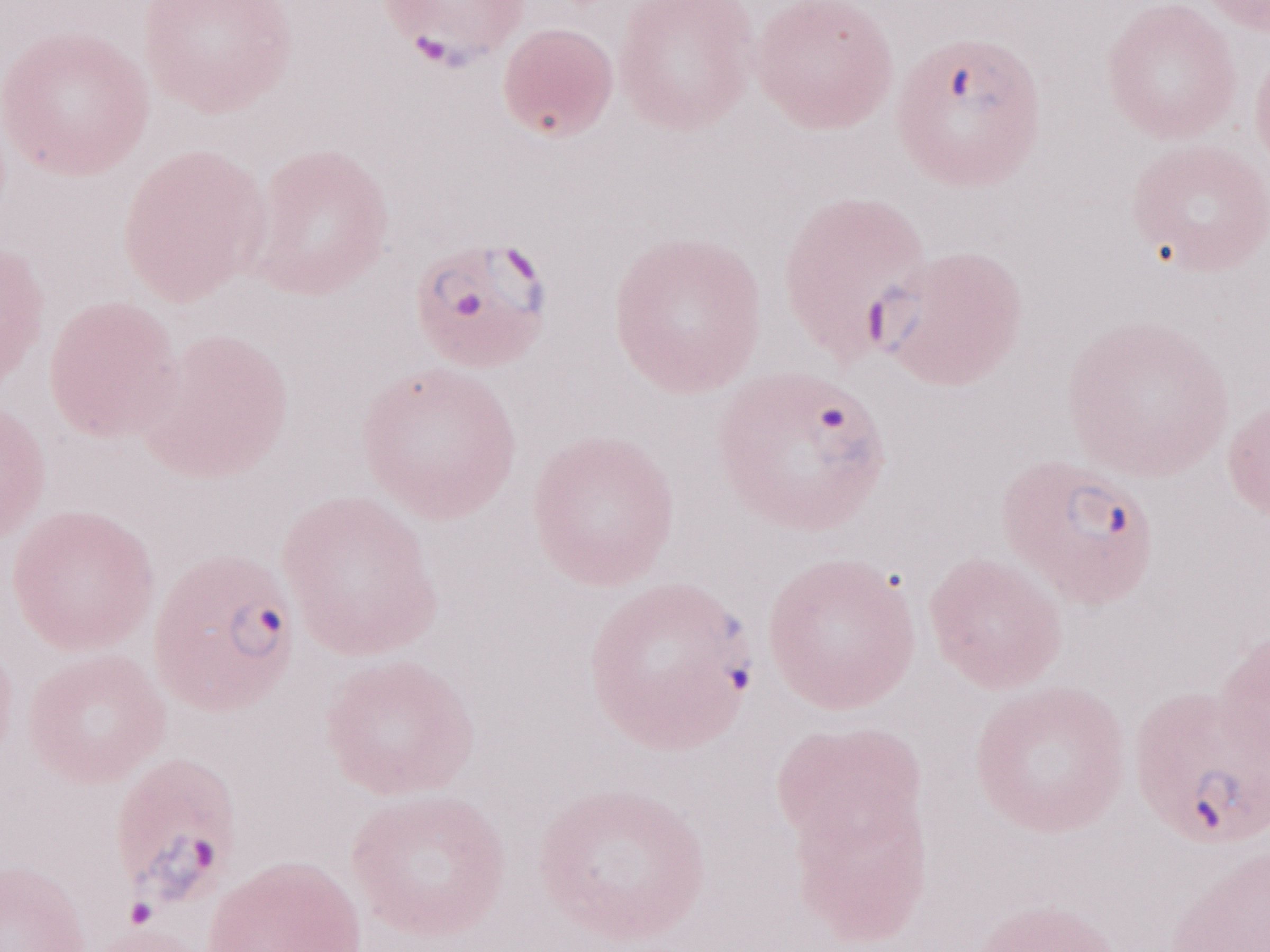

Single field of view. Olympus BX43 microscope and DP73 digital camera. Image is 1270×952 pixels. Thin blood film. 1,000x magnification. Malaria diagnosis (patient-level): positive. May-Grünwald-Giemsa stain.